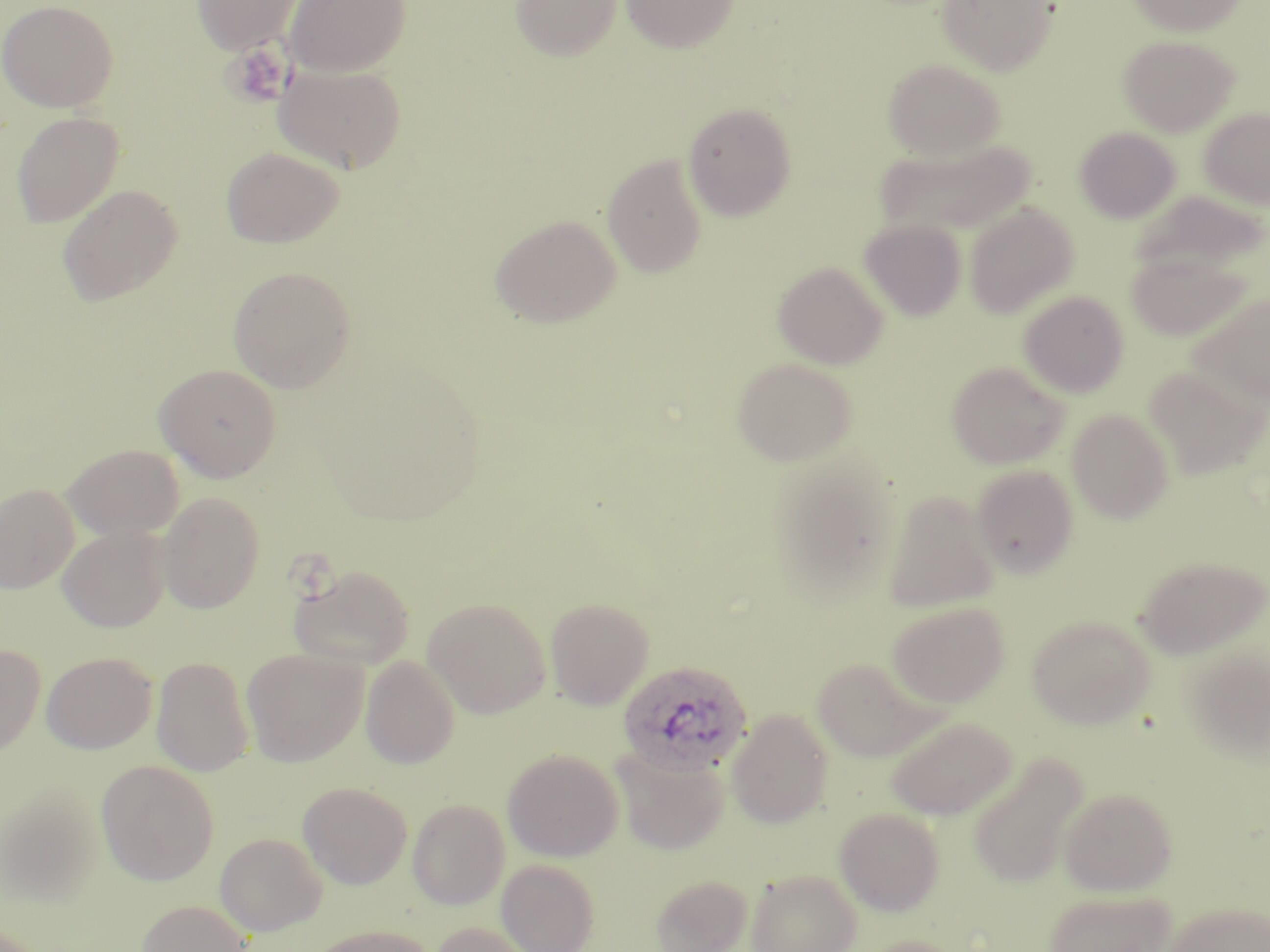

Summary:
  - Coordinate format: approximate bounding boxes as (x1, y1, x2, y2) in pixels
  - Uninfected red blood cell locations: (0, 0, 118, 113), (191, 0, 305, 56), (510, 0, 623, 61), (619, 0, 738, 53), (936, 0, 1058, 77), (1126, 0, 1247, 36), (284, 1, 412, 78), (1117, 35, 1239, 136), (882, 58, 1005, 161), (274, 64, 407, 174), (683, 102, 798, 222), (1199, 107, 1270, 211), (11, 112, 124, 228), (1074, 126, 1181, 224), (875, 137, 1036, 240), (220, 147, 344, 248), (602, 154, 707, 278), (57, 184, 183, 306), (1127, 190, 1268, 278), (965, 203, 1079, 319), (489, 215, 621, 329), (860, 220, 966, 321), (1124, 247, 1253, 343), (772, 261, 888, 369), (227, 266, 356, 392), (1188, 289, 1270, 408), (1018, 290, 1129, 397), (731, 358, 857, 466), (946, 361, 1070, 469), (154, 363, 281, 482), (1144, 363, 1268, 479), (1066, 408, 1174, 523), (62, 444, 183, 541), (970, 465, 1079, 578), (0, 483, 80, 594), (882, 490, 1000, 613), (157, 492, 265, 613), (57, 525, 170, 632), (1134, 555, 1269, 658), (289, 564, 415, 669), (422, 598, 550, 718), (545, 598, 654, 709), (886, 601, 1010, 707), (1027, 615, 1155, 729), (1185, 642, 1270, 762), (0, 644, 45, 759), (241, 649, 367, 766), (41, 652, 158, 754), (360, 655, 460, 769), (151, 657, 254, 777), (810, 657, 940, 762), (726, 709, 832, 828), (883, 715, 1018, 820), (611, 745, 730, 854), (503, 749, 623, 861), (967, 753, 1089, 888), (96, 760, 219, 885), (298, 781, 412, 889), (1, 786, 105, 906), (1059, 787, 1177, 895), (407, 799, 510, 909), (834, 807, 945, 916), (214, 832, 327, 936), (496, 859, 600, 952), (747, 869, 862, 952), (649, 874, 753, 952), (1044, 889, 1176, 952), (135, 899, 254, 952), (1162, 901, 1270, 952), (428, 921, 538, 952), (304, 924, 440, 952), (854, 935, 969, 952)
  - Platelet locations: (223, 43, 292, 106)
  - Plasmodium ovale-infected red blood cell locations: (618, 660, 752, 775)
  - Slide-level diagnosis: Plasmodium ovale
  - Modality: light microscopy
  - Image size: 1270×952 pixels
  - Stain: May-Grünwald-Giemsa
  - Preparation: thin blood film
  - Field of view: one of a larger specimen
  - Magnification: 1000x